Locate and identify every blood parasite.
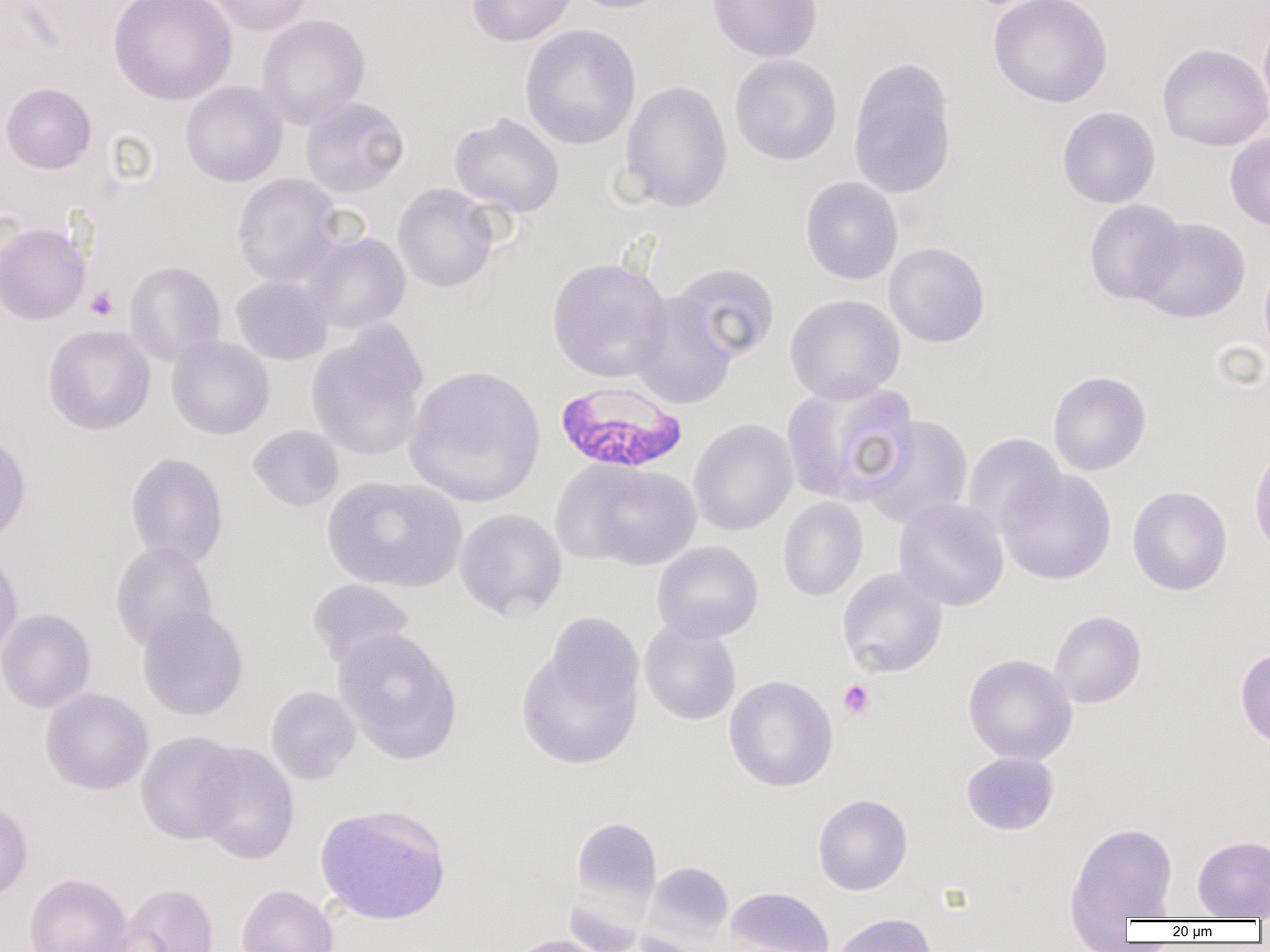
Approximate bounding boxes as (x1,y1)-(x2,y2) corner pairs in pixels.
Plasmodium falciparum-infected red blood cells: (555,382)-(688,473).
No Plasmodium ovale, Plasmodium malariae, Plasmodium vivax, Babesia divergens, or Trypanosoma brucei observed.

Uninfected red blood cell locations: (108,0)-(238,105), (206,0)-(314,35), (466,0)-(578,47), (568,0)-(677,14), (707,0)-(822,62), (988,0)-(1114,109), (257,13)-(370,128), (1258,15)-(1270,122), (519,24)-(641,150), (1157,43)-(1270,151), (729,54)-(842,166), (849,62)-(957,199), (620,80)-(733,213), (1,82)-(96,173), (181,82)-(287,187), (300,96)-(410,197), (1057,106)-(1160,208), (448,112)-(565,218), (1225,131)-(1270,231), (231,173)-(343,286), (800,177)-(903,285), (393,183)-(499,293), (1084,199)-(1187,305), (1134,217)-(1251,324), (0,221)-(91,325), (303,232)-(410,333), (884,242)-(990,348), (546,257)-(673,383), (1259,259)-(1270,368), (124,261)-(226,367), (670,263)-(781,365), (231,275)-(332,365), (630,294)-(738,409), (785,294)-(905,403), (42,324)-(155,436), (306,327)-(428,460), (166,335)-(274,440), (404,364)-(546,507), (1048,370)-(1151,476), (781,378)-(921,506), (862,415)-(974,529), (688,419)-(798,536), (248,425)-(344,511), (0,432)-(31,545), (962,433)-(1066,538), (1248,444)-(1270,556), (125,452)-(229,568), (555,459)-(703,570), (996,468)-(1117,585), (322,476)-(466,592), (1127,485)-(1233,595), (778,497)-(867,601), (893,497)-(1009,611), (454,509)-(567,621), (652,541)-(763,644), (110,542)-(217,652), (0,549)-(23,664), (836,567)-(948,678), (307,579)-(415,668), (137,605)-(248,720), (0,608)-(96,713), (1049,610)-(1147,709), (639,621)-(741,725), (332,628)-(461,763), (516,634)-(643,770), (1235,647)-(1270,752), (963,653)-(1078,765), (724,675)-(838,791), (266,686)-(360,784), (40,688)-(153,795), (136,731)-(244,845), (193,742)-(300,865), (961,751)-(1059,835), (813,793)-(912,895), (0,798)-(33,901), (315,803)-(452,926), (571,816)-(661,908), (1064,819)-(1180,927), (1192,834)-(1270,919), (644,861)-(734,943), (23,873)-(133,952), (115,882)-(220,952), (235,884)-(338,952), (725,886)-(834,952), (830,913)-(936,952), (503,934)-(614,952). Platelet locations: (85,286)-(118,320), (838,679)-(875,719). Slide-level diagnosis: Plasmodium falciparum. Optical microscopy. Thin blood smear. One field of a larger specimen. 1000x magnification. Image is 1270×952 pixels.